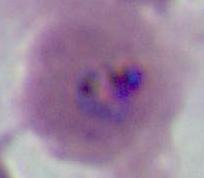
Summary:
  - Modality: photomicrograph
  - Identification: Plasmodium
  - Magnification: 400x or 1000x